Assess the morphology of the erythrocytes.
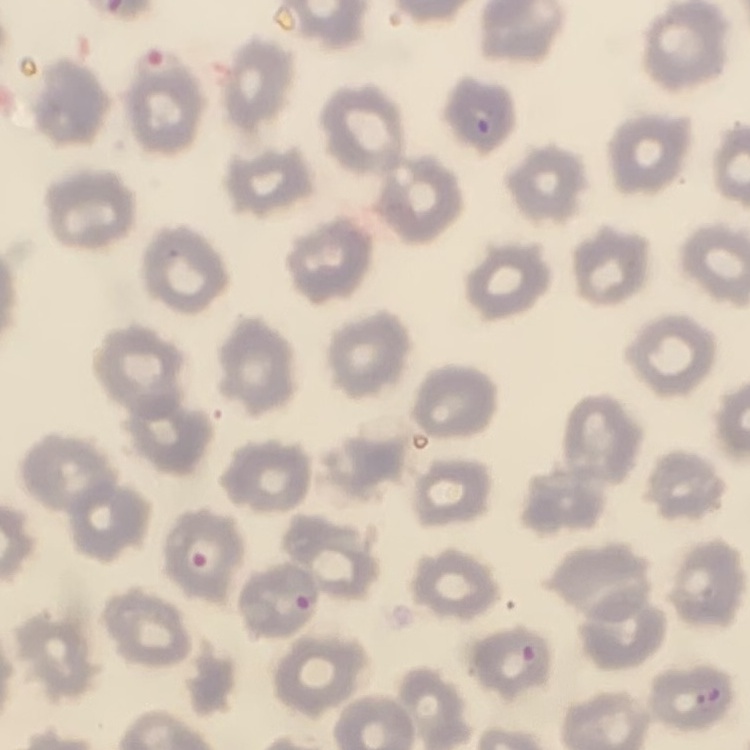

No rouleaux formation.

preparation = thin blood film
image type = square crop of a larger photomicrograph
stain = Field's or Giemsa